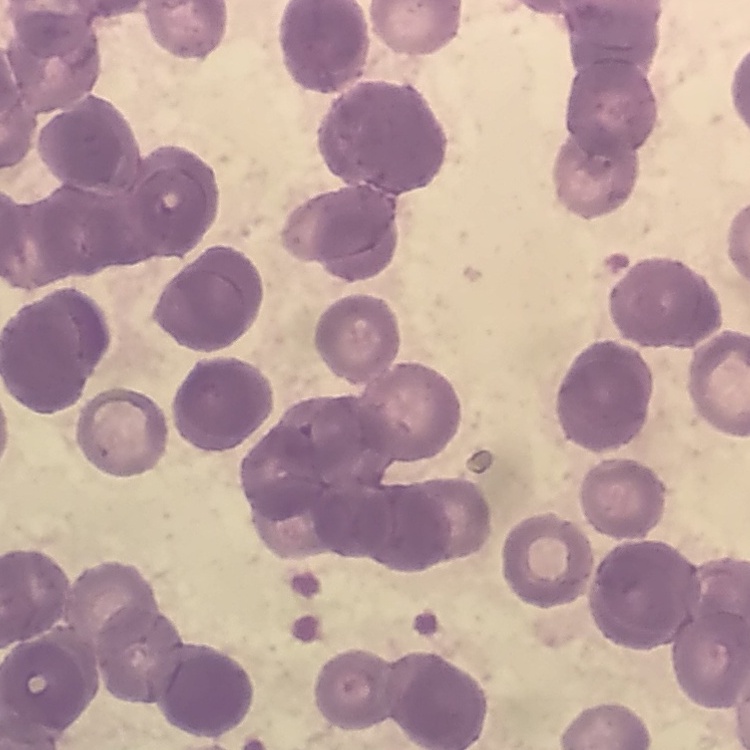

{
  "red_blood_cell_morphology": "rouleaux formation",
  "preparation": "thin peripheral smear",
  "stain": "Field's or Giemsa",
  "image_type": "one tile cut from a larger photomicrograph"
}